Classify this cell by malaria status.
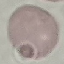
It is uninfected.

Thin smear of blood. Giemsa-stained preparation. Acquired by smartphone through the microscope eyepiece. Cell patch, automatically extracted from a larger field of view and resized to 64 × 64 pixels.